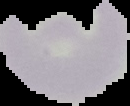

The area outside the segmented cell region is set to black. Result: no Plasmodium parasites detected. Image is 130×106 pixels. From a thin blood smear.